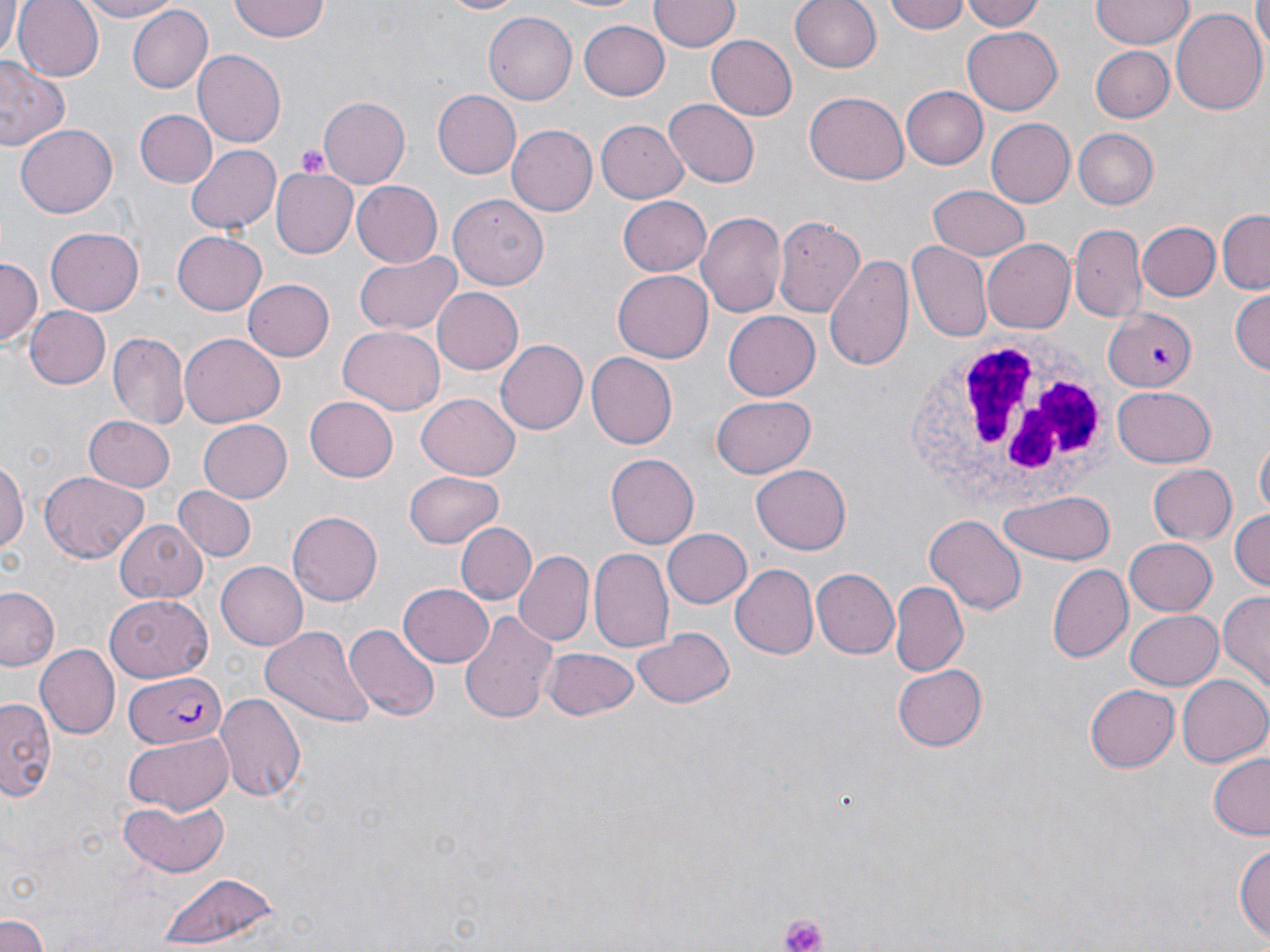 Approximate bounding boxes as [x1, y1, x2, y2] in pixels. Uninfected red blood cell locations: [0, 0, 22, 59], [12, 0, 102, 80], [70, 0, 180, 23], [230, 0, 328, 41], [432, 0, 533, 17], [546, 0, 651, 15], [649, 0, 738, 54], [788, 0, 882, 74], [883, 0, 971, 36], [962, 0, 1050, 31], [1092, 0, 1191, 49], [1254, 0, 1270, 56], [126, 5, 212, 93], [1171, 6, 1267, 118], [486, 11, 578, 104], [579, 19, 670, 100], [963, 26, 1063, 114], [705, 35, 798, 122], [1092, 45, 1174, 123], [194, 50, 286, 146], [0, 60, 69, 154], [901, 85, 988, 170], [434, 89, 524, 179], [805, 92, 909, 185], [317, 99, 410, 184], [661, 100, 759, 188], [136, 109, 216, 188], [986, 116, 1077, 208], [597, 120, 687, 202], [16, 124, 117, 219], [506, 125, 596, 216], [1073, 128, 1160, 209], [186, 144, 281, 235], [271, 164, 360, 260], [351, 180, 444, 267], [927, 184, 1031, 262], [448, 196, 549, 291], [617, 196, 711, 276], [696, 210, 786, 321], [1216, 210, 1270, 292], [773, 218, 871, 313], [1138, 222, 1220, 300], [1070, 223, 1148, 323], [45, 228, 146, 315], [172, 231, 266, 314], [983, 239, 1075, 335], [906, 241, 991, 342], [354, 251, 463, 336], [823, 251, 915, 376], [0, 255, 42, 342], [612, 269, 712, 363], [243, 279, 336, 361], [1229, 286, 1269, 376], [431, 287, 524, 374], [23, 306, 110, 389], [1104, 307, 1196, 392], [723, 311, 819, 401], [338, 324, 446, 415], [107, 330, 190, 430], [181, 334, 285, 428], [496, 339, 592, 434], [586, 352, 678, 450], [1114, 387, 1215, 466], [418, 392, 520, 479], [710, 393, 816, 479], [304, 396, 397, 482], [82, 415, 175, 492], [198, 416, 293, 501], [1256, 437, 1269, 522], [608, 453, 699, 549], [0, 456, 27, 556], [752, 463, 852, 554], [1149, 463, 1238, 546], [404, 470, 505, 547], [38, 471, 150, 562], [172, 486, 256, 563], [998, 490, 1118, 566], [1228, 507, 1269, 594], [288, 510, 383, 606], [926, 515, 1026, 616], [115, 516, 211, 603], [455, 522, 537, 606], [660, 527, 752, 610], [1124, 537, 1217, 615], [588, 549, 672, 655], [513, 551, 594, 647], [217, 561, 307, 648], [730, 563, 818, 659], [1046, 563, 1133, 664], [810, 566, 897, 660], [399, 581, 494, 667], [889, 583, 967, 678], [0, 586, 62, 672], [1218, 589, 1270, 695], [105, 593, 213, 682], [458, 610, 559, 724], [1125, 610, 1222, 690], [262, 623, 373, 729], [344, 623, 438, 721], [632, 628, 734, 709], [35, 644, 120, 739], [544, 647, 640, 721], [890, 661, 990, 753], [1175, 674, 1268, 768], [1086, 682, 1180, 770], [214, 688, 306, 800], [0, 697, 56, 799], [123, 733, 233, 813], [1207, 754, 1270, 841], [120, 799, 226, 876], [1234, 837, 1270, 948], [150, 870, 282, 949], [0, 913, 49, 951]. Platelet locations: [292, 144, 331, 177], [781, 914, 826, 952]. Plasmodium falciparum-infected red blood cell locations: [124, 671, 230, 746]. White blood cell locations: [906, 331, 1114, 521]. Slide-level diagnosis: Plasmodium falciparum. May-Grünwald-Giemsa-stained preparation. 1000x magnification. Thin blood smear. Light microscopy. Image is 1270×952 pixels. One field of a larger specimen.